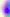
Summary:
  - Identification: Toxoplasma gondii
  - Magnification: 400x
  - Modality: photomicrograph